State the blood parasite species.
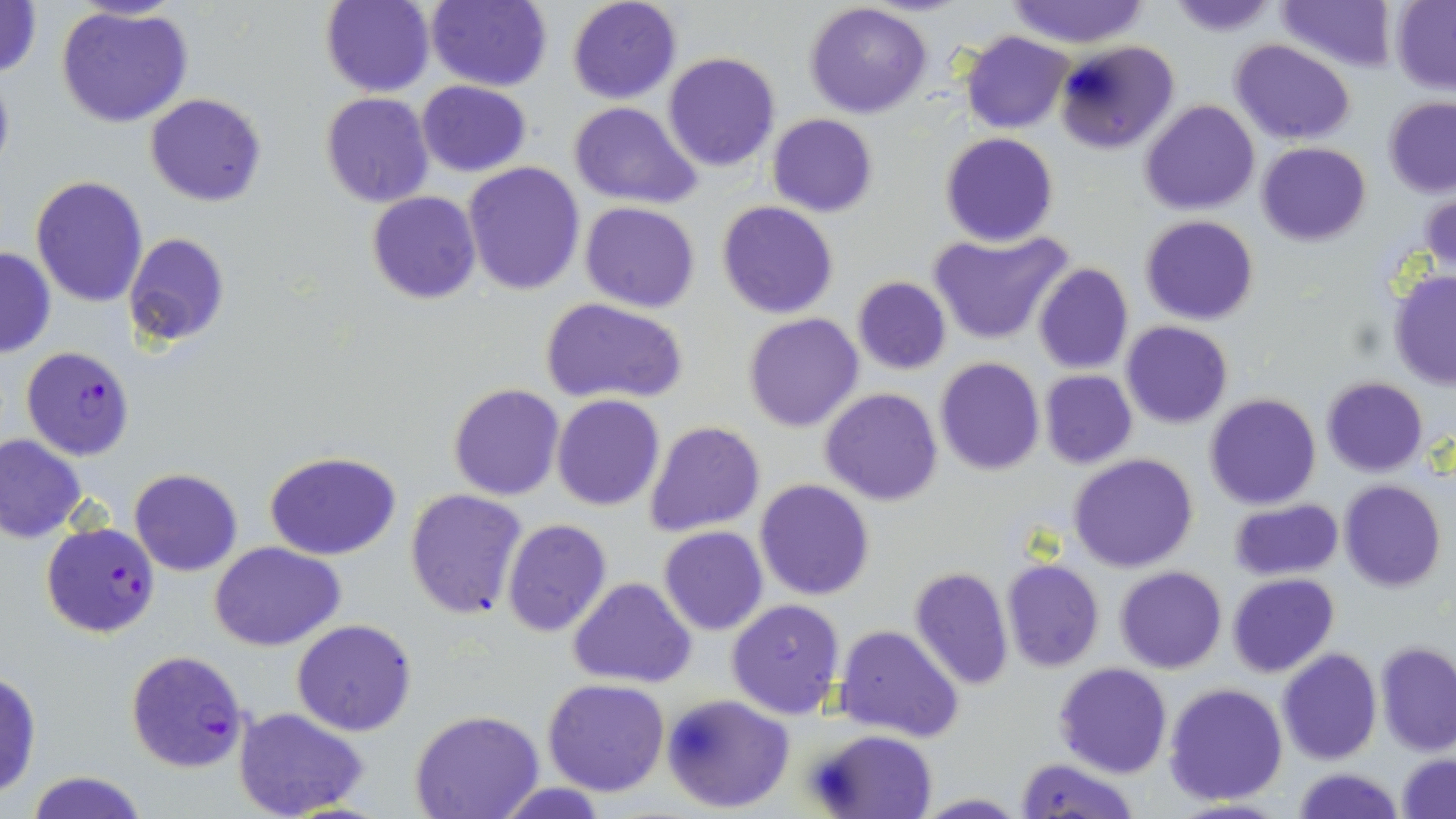
Plasmodium falciparum.

Summary:
  - Coordinate format: approximate bounding boxes as named x1/y1/x2/y2 corners in pixels
  - Uninfected red blood cell locations: (x1=0, y1=0, x2=44, y2=80), (x1=66, y1=0, x2=184, y2=21), (x1=320, y1=0, x2=435, y2=97), (x1=423, y1=0, x2=553, y2=91), (x1=567, y1=0, x2=682, y2=104), (x1=1167, y1=0, x2=1280, y2=38), (x1=1276, y1=0, x2=1398, y2=71), (x1=1005, y1=1, x2=1151, y2=48), (x1=1390, y1=1, x2=1456, y2=92), (x1=804, y1=2, x2=933, y2=118), (x1=57, y1=6, x2=192, y2=129), (x1=960, y1=30, x2=1073, y2=133), (x1=1053, y1=39, x2=1179, y2=154), (x1=1230, y1=39, x2=1355, y2=145), (x1=662, y1=52, x2=781, y2=172), (x1=0, y1=63, x2=15, y2=181), (x1=416, y1=80, x2=532, y2=178), (x1=319, y1=92, x2=434, y2=206), (x1=144, y1=93, x2=267, y2=207), (x1=1383, y1=97, x2=1456, y2=197), (x1=1139, y1=100, x2=1260, y2=215), (x1=567, y1=101, x2=700, y2=207), (x1=766, y1=114, x2=878, y2=217), (x1=939, y1=133, x2=1059, y2=247), (x1=1257, y1=142, x2=1370, y2=246), (x1=461, y1=162, x2=586, y2=296), (x1=30, y1=174, x2=150, y2=307), (x1=366, y1=190, x2=481, y2=305), (x1=1422, y1=192, x2=1456, y2=274), (x1=716, y1=200, x2=838, y2=319), (x1=579, y1=201, x2=701, y2=313), (x1=1140, y1=215, x2=1259, y2=325), (x1=928, y1=230, x2=1073, y2=346), (x1=122, y1=232, x2=231, y2=350), (x1=0, y1=246, x2=55, y2=359), (x1=1033, y1=263, x2=1133, y2=376), (x1=1389, y1=271, x2=1456, y2=388), (x1=851, y1=277, x2=952, y2=374), (x1=541, y1=298, x2=690, y2=406), (x1=741, y1=312, x2=863, y2=433), (x1=1121, y1=321, x2=1233, y2=428), (x1=934, y1=357, x2=1045, y2=475), (x1=1039, y1=370, x2=1137, y2=470), (x1=1321, y1=376, x2=1429, y2=477), (x1=446, y1=383, x2=564, y2=501), (x1=820, y1=387, x2=944, y2=507), (x1=1206, y1=393, x2=1321, y2=510), (x1=551, y1=395, x2=665, y2=511), (x1=642, y1=420, x2=766, y2=536), (x1=0, y1=434, x2=85, y2=542), (x1=263, y1=450, x2=404, y2=561), (x1=1069, y1=454, x2=1198, y2=573), (x1=129, y1=467, x2=243, y2=577), (x1=753, y1=479, x2=877, y2=602), (x1=1339, y1=480, x2=1445, y2=592), (x1=405, y1=489, x2=528, y2=620), (x1=1227, y1=499, x2=1343, y2=581), (x1=502, y1=519, x2=612, y2=637), (x1=658, y1=526, x2=769, y2=636), (x1=210, y1=541, x2=346, y2=650), (x1=1000, y1=558, x2=1104, y2=672), (x1=908, y1=566, x2=1013, y2=690), (x1=1116, y1=566, x2=1227, y2=673), (x1=1227, y1=573, x2=1339, y2=677), (x1=568, y1=577, x2=695, y2=687), (x1=726, y1=598, x2=848, y2=720), (x1=291, y1=619, x2=417, y2=737), (x1=835, y1=625, x2=964, y2=744), (x1=1377, y1=642, x2=1456, y2=756), (x1=1277, y1=648, x2=1382, y2=765), (x1=1054, y1=662, x2=1172, y2=779), (x1=0, y1=671, x2=41, y2=799), (x1=542, y1=678, x2=670, y2=797), (x1=1164, y1=682, x2=1288, y2=805), (x1=661, y1=694, x2=795, y2=815), (x1=233, y1=708, x2=369, y2=819), (x1=410, y1=711, x2=544, y2=819), (x1=810, y1=729, x2=937, y2=819), (x1=1397, y1=753, x2=1456, y2=819), (x1=1015, y1=757, x2=1139, y2=819), (x1=1294, y1=767, x2=1401, y2=819), (x1=25, y1=770, x2=147, y2=819), (x1=915, y1=794, x2=1029, y2=817)
  - Plasmodium falciparum-infected red blood cell locations: (x1=20, y1=346, x2=135, y2=460), (x1=41, y1=522, x2=160, y2=639), (x1=125, y1=649, x2=250, y2=775)
  - Magnification: 1000x
  - Modality: optical microscopy
  - Stain: May-Grünwald-Giemsa
  - Image size: 1456×819 pixels
  - Preparation: thin blood smear
  - Field of view: single